Give the position of every leukocyte visible.
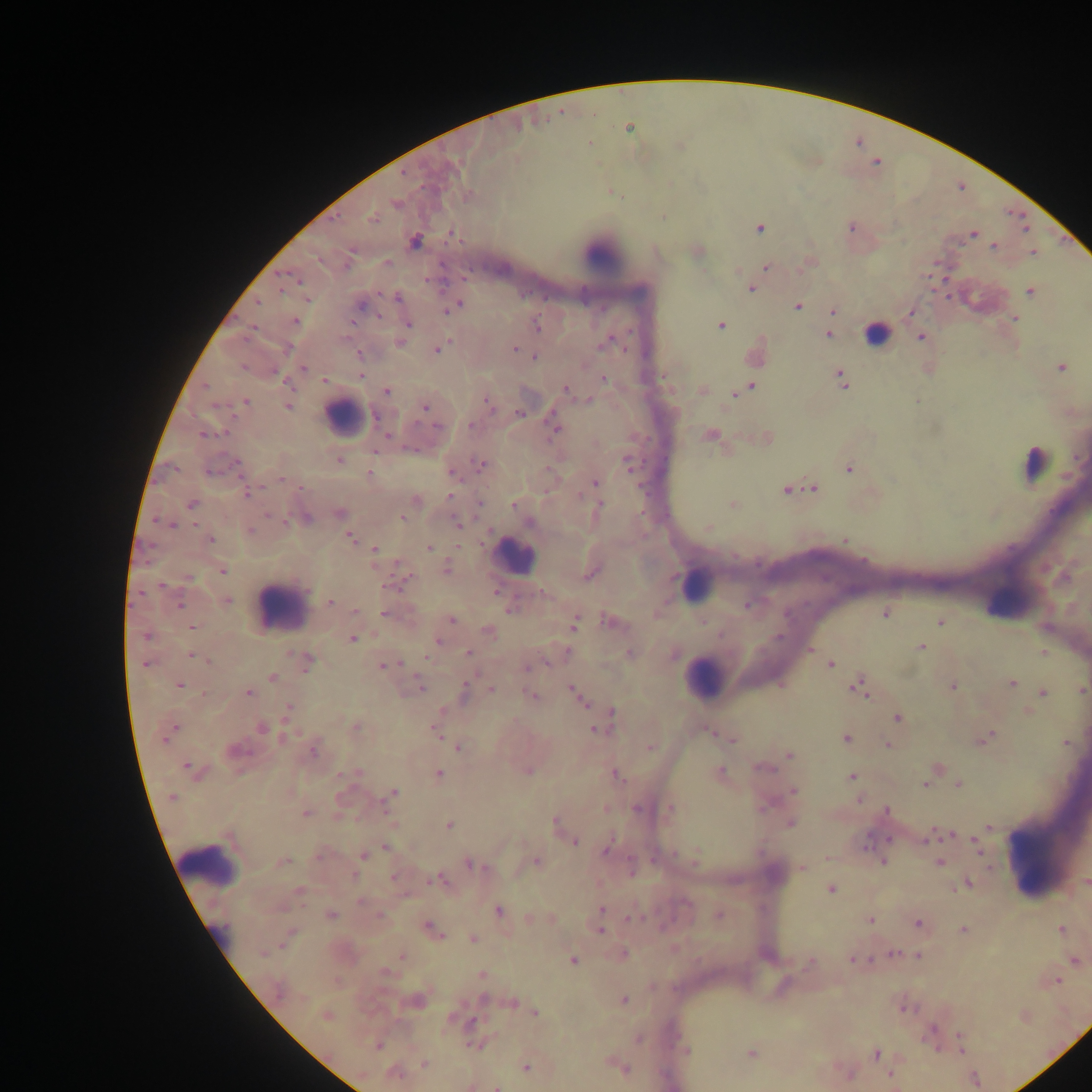

Approximate centers as x y in pixels.
Leukocytes: 601 253; 978 299; 877 334; 344 416; 1034 463; 514 556; 697 584; 280 606; 703 677; 1042 856; 209 863.

Malaria parasite locations: 628 127; 372 217; 850 227; 759 228; 974 234; 415 242; 993 245; 697 250; 1032 252; 386 263; 766 266; 751 288; 1029 290; 396 297; 360 303; 456 305; 797 305; 833 310; 911 312; 1014 319; 295 321; 407 324; 719 325; 536 326; 828 333; 921 337; 400 342; 606 342; 436 349; 514 349; 358 353; 755 354; 534 357; 1061 367; 303 368; 360 376; 664 376; 603 378; 841 379; 324 380; 751 387; 565 390; 703 390; 742 390; 386 391; 735 393; 586 400; 245 402; 488 402; 287 405; 424 406; 519 414; 437 426; 553 426; 206 434; 709 434; 766 438; 339 460; 481 464; 237 465; 629 465; 848 467; 451 471; 370 473; 595 482; 786 488; 813 488; 247 493; 450 496; 415 501; 191 504; 515 504; 732 505; 598 508; 339 513; 403 517; 304 518; 458 524; 708 527; 249 531; 350 537; 211 539; 844 540; 429 548; 375 554; 447 569; 223 570; 590 573; 405 576; 226 600; 330 603; 747 605; 355 611; 884 612; 385 613; 451 620; 610 621; 939 621; 573 623; 193 626; 488 631; 147 636; 351 639; 437 640; 921 646; 809 649; 469 653; 629 653; 674 653; 1042 653; 192 655; 306 662; 146 663; 829 664; 383 665; 527 667; 272 677; 1011 683; 178 684; 420 685; 858 685; 952 686; 492 689; 573 690; 1082 690; 464 691; 248 692; 1042 692; 531 696; 580 699; 1028 711; 286 713; 610 713; 897 718; 262 727; 355 727; 597 728; 436 729; 169 731; 711 732; 985 738; 732 739; 846 739; 1065 743; 887 744; 458 747; 650 747; 313 750; 235 751; 788 755; 936 767; 192 770; 526 770; 354 773; 438 773; 614 773; 720 773; 852 776; 959 783; 926 784; 792 791; 392 793; 172 797; 859 798; 605 808; 669 808; 886 810; 306 813; 789 822; 393 824; 556 824; 448 825; 989 828; 945 834; 933 836; 972 838; 574 841; 977 845; 385 847; 607 847; 362 854; 696 854; 320 856; 827 857; 536 861; 883 861; 282 862; 470 863; 939 863; 631 868; 801 868; 394 877; 440 879; 1086 882; 966 883; 830 889; 299 892; 360 901; 602 909; 498 911; 330 915; 717 915; 530 918; 600 918; 630 918; 550 919; 870 919; 917 924; 431 928; 600 930; 963 930; 1061 930; 287 938; 473 938; 892 954; 621 955; 403 956; 917 956; 852 959; 572 960; 1075 960; 810 963; 481 974; 1055 981; 623 999; 415 1000; 511 1002; 903 1006; 534 1012; 325 1015; 1023 1016; 960 1037; 638 1039; 475 1043; 378 1045; 686 1051; 750 1053; 875 1053; 424 1065; 525 1066; 621 1068; 394 1073; 846 1073; 889 1074; 472 1085; 497 1086. Image is 1092×1092 pixels. Thick blood smear. One field of view. Collected in Ghana. Photographed through a microscope with a mobile-phone camera.